Report the malaria status of this cell.
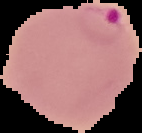
Parasitized.

preparation: thin blood smear
image_type: segmented cell region with the area outside set to black
image_size: 142×133 pixels